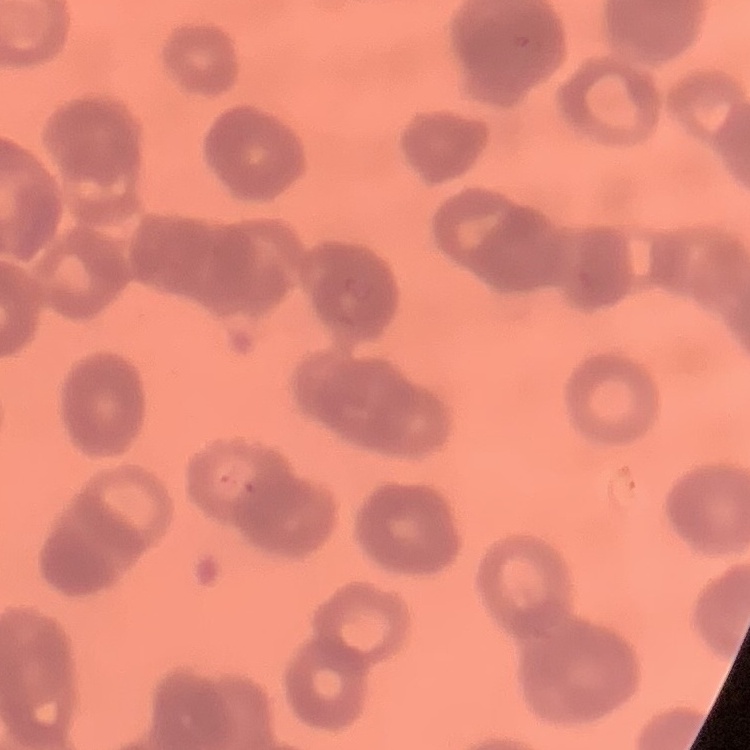 The red blood cells exhibit rouleaux formation. Thin blood smear. Square crop of a larger photomicrograph. Stained with either Field's or Giemsa.